Classify this cell by malaria status.
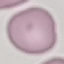
Uninfected.

preparation = thin blood smear
stain = Giemsa
image type = automatically extracted cell patch, resized to 64 × 64 pixels
capture = smartphone camera at the microscope eyepiece